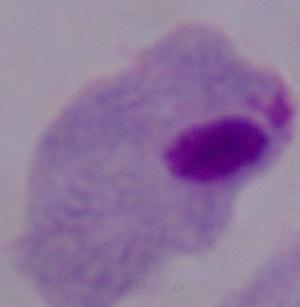

Summary:
  - Identification: trichomonad
  - Magnification: 1000x
  - Modality: photomicrograph